Identify the parasite.
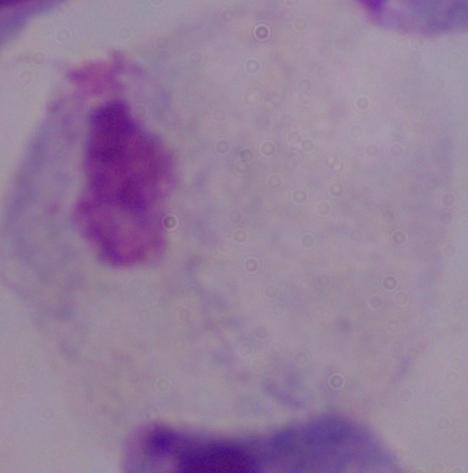

This is a trichomonad.

{
  "magnification": "1000x",
  "modality": "photomicrograph"
}